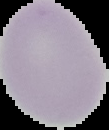
preparation: thin blood film
malaria_status: uninfected
image_size: 109×130 pixels
image_type: cell region segmented out of the field of view; surrounding area masked to black